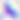
magnification = 400x
modality = micrograph
identification = Toxoplasma gondii